Identify the cell.
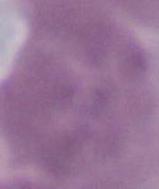

An erythrocyte.

Summary:
  - Magnification: 1000x
  - Modality: photomicrograph